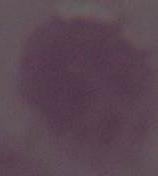

identification: red blood cell
modality: micrograph
magnification: 1000x